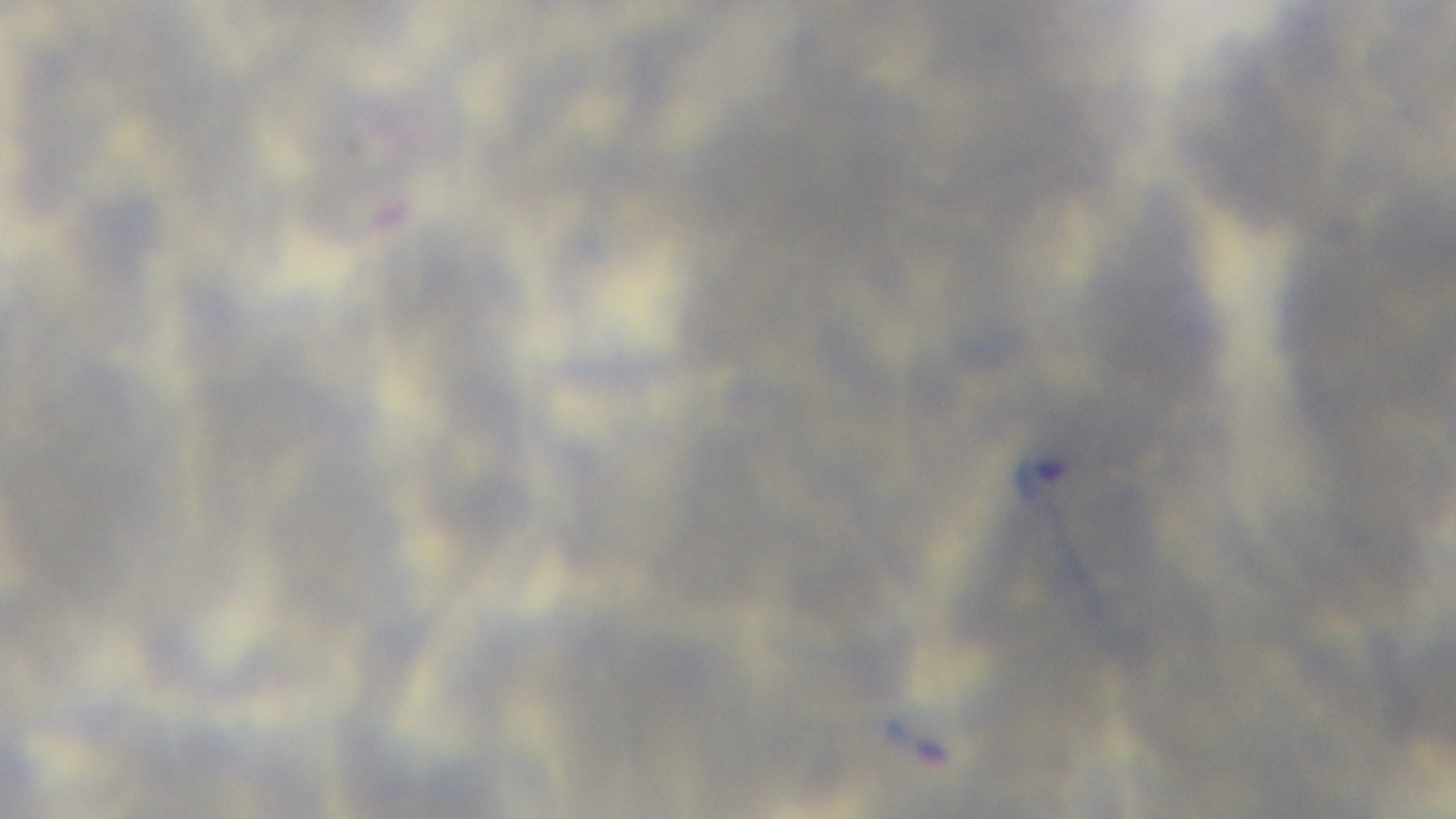
Malaria status: infected. Mounted 4K digital camera. Oil-immersion objective, 100x. Single field of view. Photomicrograph. Preparation: thin blood film. Giemsa stain.